Classify this cell by malaria status.
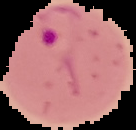
It is parasitized.

image type = segmented cell region with the area outside set to black
preparation = thin blood film
image size = 136×130 pixels